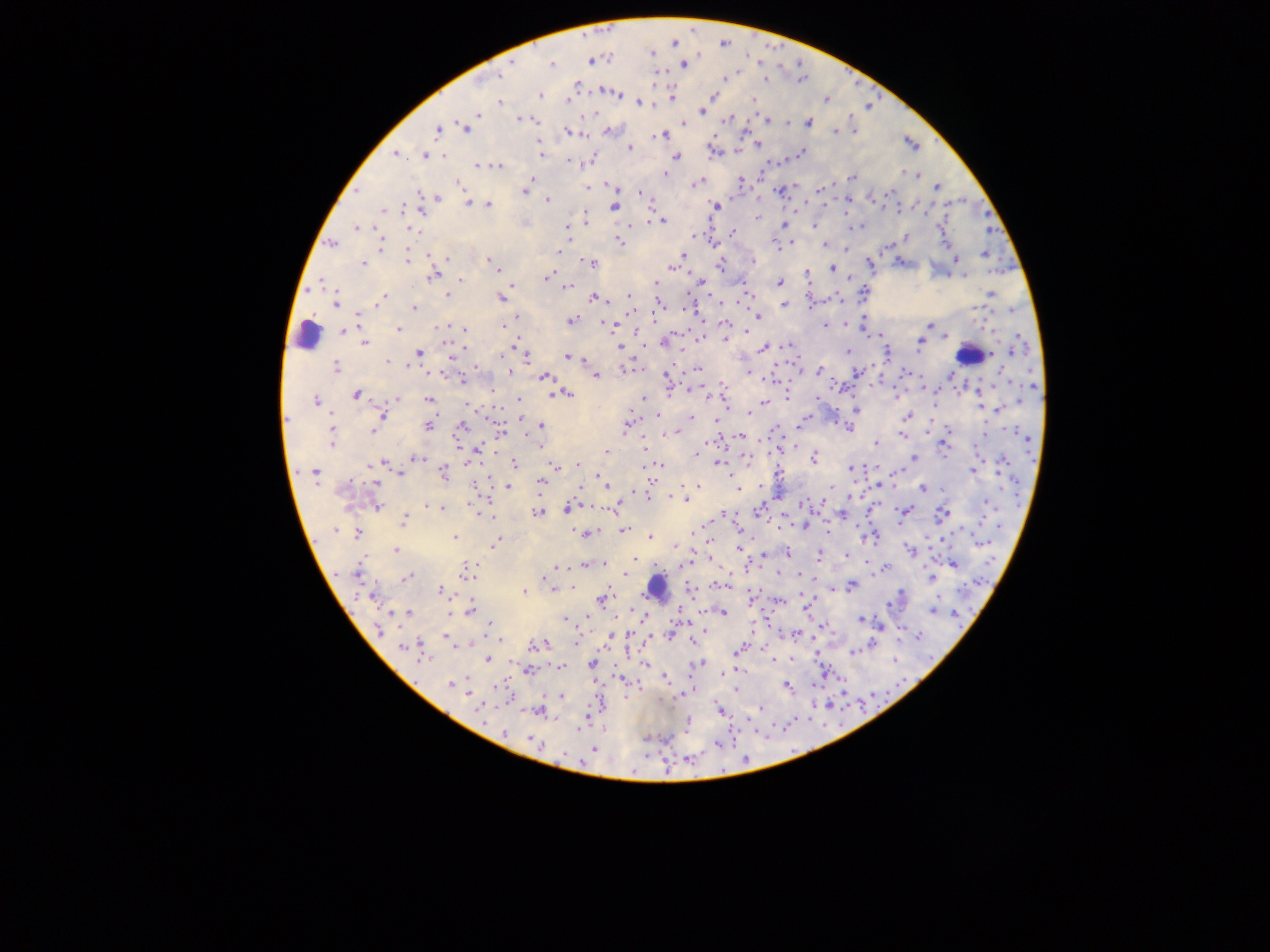

Approximate centers as x y in pixels.
Summary:
  - Leukocyte locations: 307 335; 967 355; 656 586
  - Malaria parasite locations: 605 29; 695 32; 584 35; 725 41; 674 42; 767 44; 781 47; 652 52; 698 54; 746 54; 609 58; 590 60; 514 62; 760 62; 802 62; 551 64; 683 64; 737 71; 845 72; 655 73; 498 76; 725 77; 767 78; 799 81; 853 82; 575 85; 604 91; 613 93; 877 93; 540 95; 713 95; 671 96; 567 98; 753 100; 825 100; 500 102; 639 102; 869 108; 702 110; 585 113; 476 114; 851 116; 520 117; 727 118; 535 120; 748 120; 765 120; 724 121; 787 121; 806 122; 683 123; 464 127; 437 129; 853 130; 608 131; 745 131; 836 131; 566 132; 713 133; 662 135; 936 138; 537 141; 758 144; 912 144; 630 148; 712 151; 738 151; 395 153; 799 153; 424 154; 441 154; 541 155; 677 156; 588 160; 786 160; 568 162; 768 162; 477 165; 482 165; 498 166; 900 172; 663 174; 917 175; 853 177; 531 178; 759 178; 741 180; 457 182; 697 182; 833 183; 588 185; 613 186; 937 187; 797 188; 819 188; 356 189; 778 190; 751 191; 524 193; 639 193; 887 193; 732 194; 418 195; 871 197; 961 197; 436 198; 758 198; 545 200; 405 203; 469 203; 948 203; 488 205; 809 205; 844 205; 614 206; 715 206; 826 206; 420 207; 911 208; 924 208; 382 209; 897 209; 796 212; 983 214; 584 217; 757 217; 708 219; 660 220; 650 221; 634 223; 783 224; 814 224; 857 225; 566 226; 938 226; 357 228; 376 228; 990 228; 410 229; 732 233; 693 236; 905 238; 710 239; 569 240; 618 241; 332 243; 790 243; 944 243; 824 244; 776 245; 889 245; 380 246; 846 250; 560 251; 429 253; 684 255; 983 255; 446 256; 999 256; 407 257; 954 257; 488 259; 751 261; 899 261; 589 262; 362 263; 869 264; 720 265; 672 266; 831 268; 1002 272; 433 274; 806 274; 963 275; 548 277; 949 277; 849 278; 460 279; 701 281; 778 282; 655 284; 513 285; 743 285; 568 286; 311 288; 864 292; 991 294; 747 295; 447 296; 383 297; 502 297; 593 297; 630 297; 838 298; 715 301; 823 301; 335 302; 658 304; 783 305; 811 306; 978 306; 414 307; 687 308; 1011 310; 761 313; 359 316; 757 316; 517 317; 986 319; 570 320; 863 320; 726 321; 845 321; 702 322; 604 323; 448 324; 613 325; 504 326; 824 326; 929 326; 436 328; 398 329; 464 330; 344 331; 748 331; 639 332; 676 333; 868 334; 1015 334; 698 336; 876 336; 947 337; 724 338; 665 341; 447 342; 920 343; 364 344; 787 345; 513 347; 619 347; 762 347; 682 348; 1026 348; 1013 351; 418 352; 847 352; 886 352; 567 356; 991 356; 583 358; 453 359; 527 359; 385 361; 791 361; 670 362; 871 363; 335 367; 473 367; 627 367; 698 368; 684 370; 819 370; 510 371; 748 371; 1001 371; 443 372; 904 372; 801 373; 856 373; 950 375; 595 376; 544 377; 666 378; 769 378; 834 378; 463 379; 879 380; 721 381; 923 385; 995 385; 1033 385; 700 386; 851 386; 960 387; 688 389; 979 389; 491 393; 667 393; 937 393; 566 394; 356 395; 552 395; 894 395; 314 396; 709 396; 813 396; 978 396; 645 397; 787 397; 397 398; 1043 399; 428 400; 520 400; 1019 400; 724 401; 764 403; 470 406; 834 406; 980 407; 998 408; 856 411; 331 412; 748 412; 381 415; 657 416; 908 416; 520 417; 692 417; 715 418; 804 418; 933 419; 285 421; 837 422; 799 423; 626 424; 428 425; 541 425; 461 426; 849 427; 952 428; 1012 429; 330 430; 373 430; 499 430; 775 430; 677 431; 459 432; 928 432; 984 434; 902 435; 331 436; 740 436; 721 437; 1027 438; 707 441; 456 442; 876 442; 794 444; 943 444; 643 445; 541 446; 780 447; 977 447; 475 449; 607 451; 494 454; 696 455; 415 457; 744 457; 914 458; 947 458; 471 459; 720 459; 813 459; 384 462; 514 463; 577 464; 1000 464; 656 465; 661 465; 879 466; 556 467; 852 468; 973 470; 297 472; 313 472; 400 473; 443 473; 899 473; 779 474; 600 475; 488 479; 760 480; 852 480; 1012 480; 540 481; 376 482; 649 482; 474 483; 605 484; 698 485; 507 486; 878 486; 895 486; 829 487; 738 488; 922 488; 945 488; 580 490; 1003 490; 634 491; 647 492; 1018 493; 489 494; 675 497; 778 497; 849 497; 683 498; 862 498; 985 501; 807 502; 821 502; 583 503; 618 504; 798 504; 376 505; 426 505; 891 507; 1019 507; 441 508; 567 509; 604 509; 868 509; 905 510; 761 511; 814 511; 475 512; 539 513; 724 513; 842 513; 943 513; 494 515; 729 516; 826 519; 981 519; 402 521; 871 522; 900 522; 938 522; 779 523; 707 524; 806 525; 962 525; 855 526; 997 527; 570 528; 741 529; 337 530; 624 530; 600 531; 829 531; 696 532; 356 533; 583 533; 957 534; 970 534; 650 535; 755 535; 861 535; 316 537; 453 537; 874 537; 926 539; 941 540; 496 542; 981 543; 675 546; 709 546; 739 549; 911 549; 397 550; 788 553; 819 554; 764 555; 846 555; 633 558; 711 559; 747 560; 603 563; 985 563; 683 564; 869 564; 925 564; 953 564; 584 565; 558 566; 759 566; 885 567; 333 571; 467 571; 778 571; 357 572; 552 572; 624 573; 798 574; 407 577; 931 578; 813 580; 708 584; 721 584; 977 584; 550 585; 852 586; 958 586; 901 587; 552 589; 690 589; 764 589; 832 589; 440 590; 524 590; 800 591; 373 594; 354 595; 601 598; 750 600; 779 600; 939 600; 807 605; 888 605; 633 607; 470 608; 932 610; 393 612; 955 612; 350 613; 407 613; 449 613; 722 613; 566 619; 646 619; 861 619; 679 622; 769 624; 821 625; 489 626; 880 627; 753 629; 380 630; 701 630; 670 632; 900 632; 631 633; 797 633; 610 636; 918 636; 448 637; 502 637; 816 637; 694 639; 646 640; 471 643; 538 644; 576 644; 872 645; 403 646; 409 646; 762 647; 627 648; 417 649; 553 650; 739 650; 895 653; 853 654; 790 655; 817 655; 925 656; 423 657; 487 660; 688 660; 773 661; 645 663; 700 663; 591 664; 547 665; 561 667; 739 668; 528 669; 825 670; 468 672; 725 673; 842 677; 619 678; 664 678; 595 680; 451 684; 813 684; 899 684; 787 685; 501 686; 691 688; 736 689; 842 690; 682 693; 561 695; 872 695; 859 703; 814 705; 829 705; 480 706; 602 706; 718 708; 760 708; 538 710; 756 711; 586 714; 690 716; 808 721; 825 722; 789 723; 730 727; 741 727; 687 728; 505 733; 647 737; 664 737; 771 737; 534 742; 717 744; 593 748; 564 753; 649 753; 686 756; 745 757; 667 758
  - Country: Ghana
  - Image size: 1270×952 pixels
  - Preparation: thick blood film
  - Capture: mobile-phone photograph through a microscope
  - Field of view: single